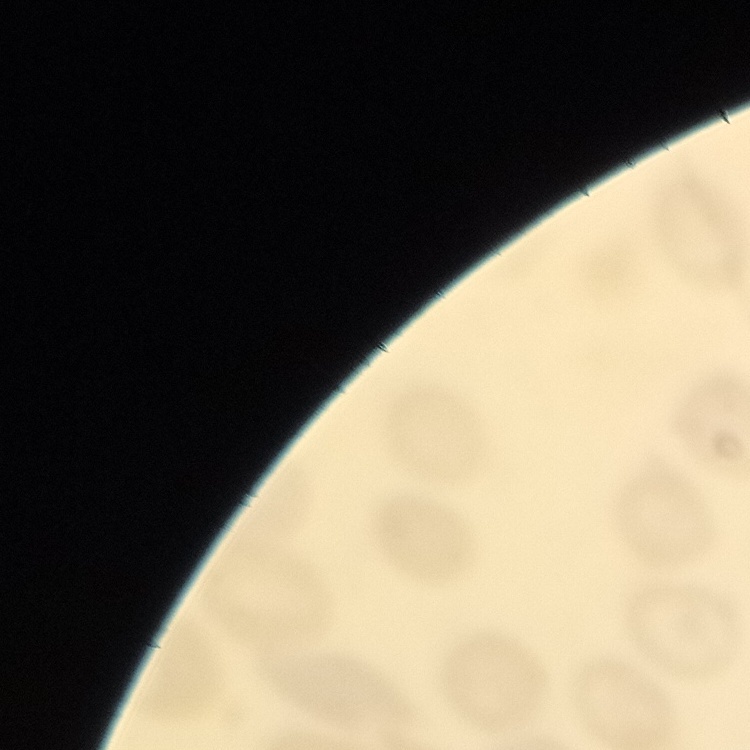
Summary:
  - Erythrocyte morphology: no rouleaux formation
  - Image type: one tile cut from a larger photomicrograph
  - Preparation: thin peripheral smear
  - Stain: Field's or Giemsa